Classify this cell by malaria status.
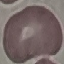

Uninfected.

Thin blood film. Cell patch, automatically extracted from a larger field of view and resized to 64 × 64 pixels. Giemsa-stained preparation. Photographed with a smartphone camera at the microscope eyepiece.